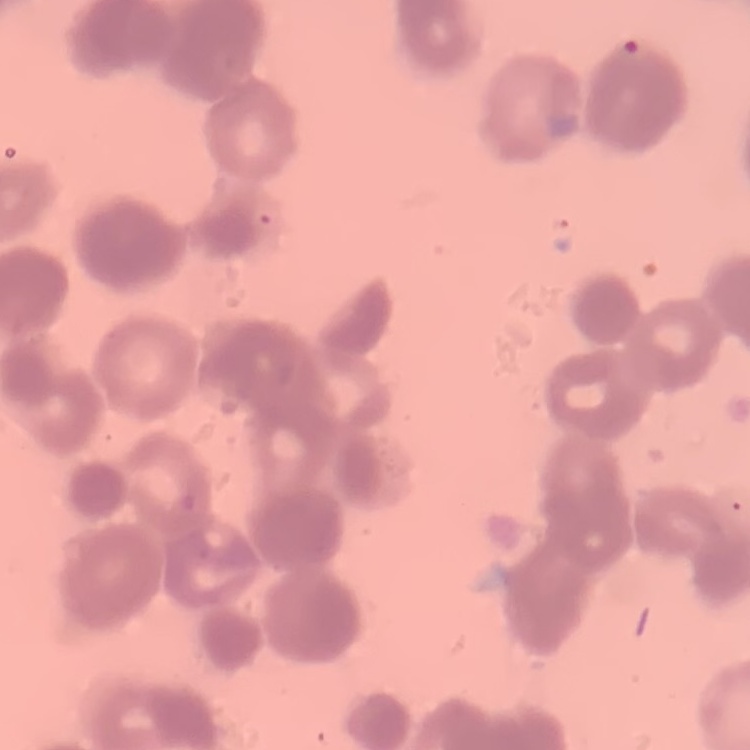

{
  "erythrocyte_morphology": "rouleaux formation",
  "preparation": "thin blood film",
  "stain": "Field's or Giemsa",
  "image_type": "one tile cut from a larger photomicrograph"
}